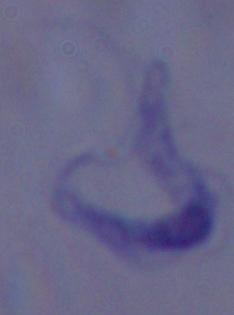

magnification = 1000x
modality = photomicrograph
identification = trypanosome